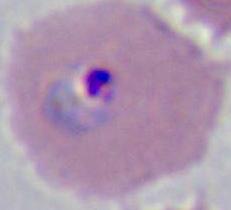

Summary:
  - Modality: photomicrograph
  - Identification: Plasmodium
  - Magnification: 400x or 1000x